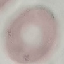

result: no malaria parasites detected
capture: smartphone through the microscope eyepiece
preparation: thin smear
stain: Giemsa
image_type: cell patch, automatically extracted from a larger field of view and resized to 64 × 64 pixels